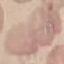

Summary:
  - Malaria status: uninfected
  - Capture: smartphone camera at the microscope eyepiece
  - Preparation: thin blood film
  - Stain: Giemsa
  - Image type: automatically extracted cell patch, resized to 64 × 64 pixels